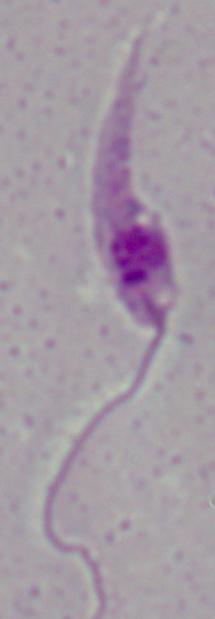 Micrograph. A Leishmania parasite is seen. Captured at 1000x magnification.